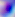
Micrograph. 400x magnification. Toxoplasma gondii is seen.